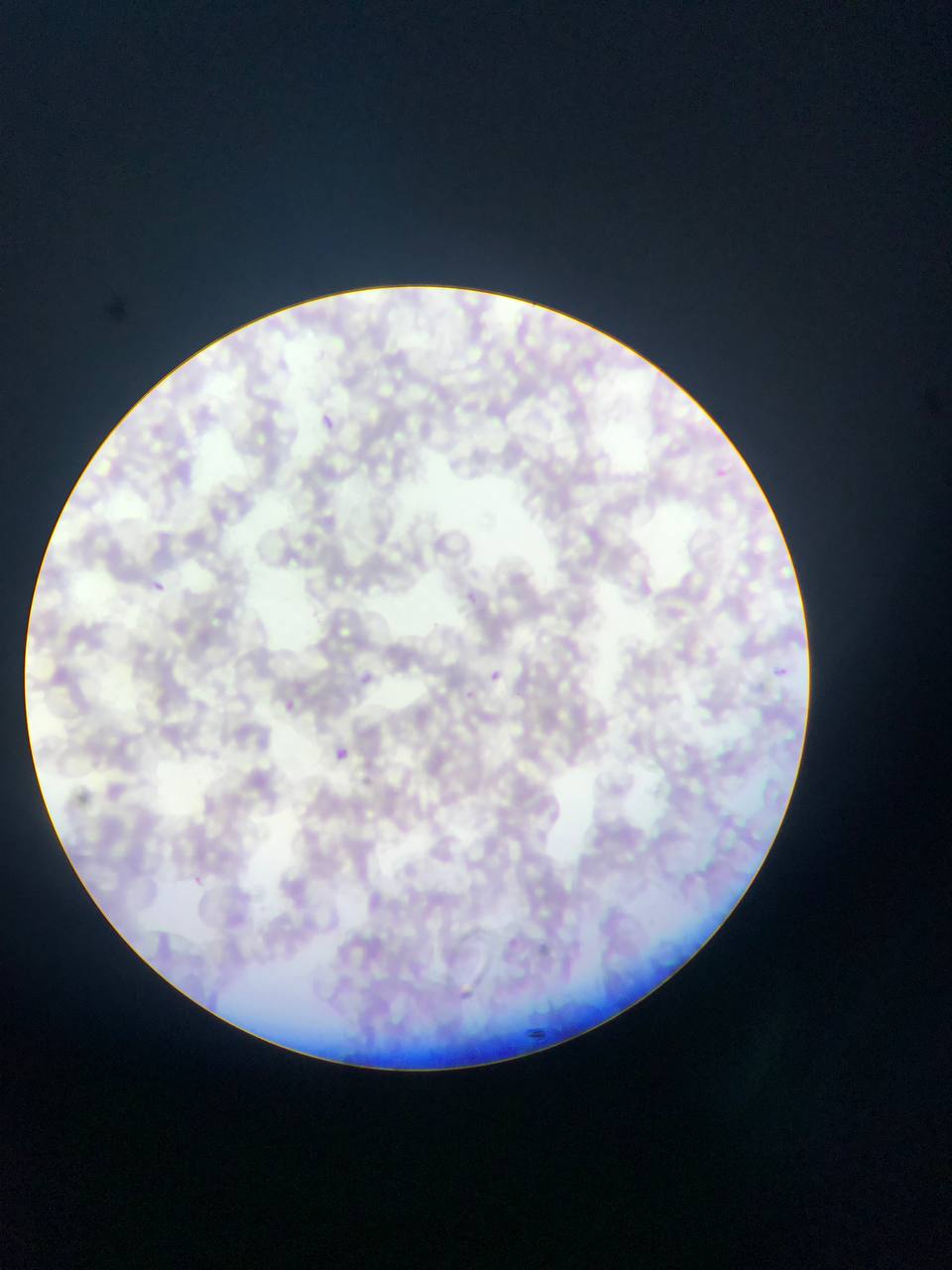
country = Ghana
malaria parasite locations = approximate bounding boxes as left top right bottom in pixels: 314 408 343 435; 706 462 733 486; 151 576 165 594; 466 589 478 601; 483 665 507 688; 773 665 788 679; 278 695 301 718; 333 747 349 763; 187 871 207 890
field of view = single
preparation = thin blood film
image size = 952×1270 pixels
capture = mobile-phone photograph through a microscope